Locate and identify every blood parasite.
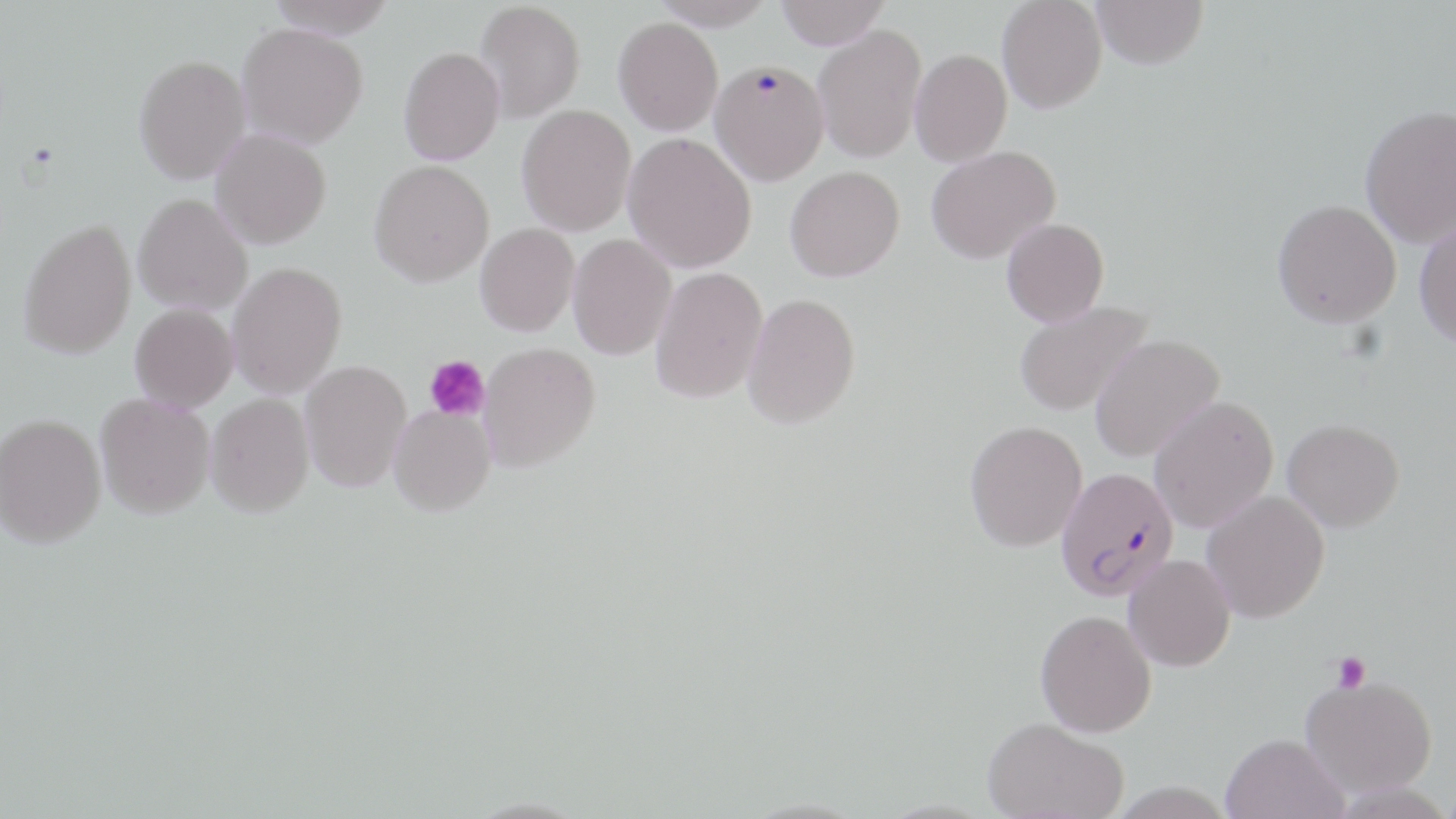

Approximate bounding boxes as named x1/y1/x2/y2 corners in pixels.
Plasmodium falciparum-infected red blood cells: (x1=1056, y1=466, x2=1178, y2=600).
No Plasmodium ovale, Plasmodium malariae, Plasmodium vivax, Babesia divergens, or Trypanosoma brucei observed.

{
  "slide_level_diagnosis": "Plasmodium falciparum",
  "field_of_view": "single",
  "image_size": "1456×819 pixels",
  "platelet_locations": "approximate bounding boxes as named x1/y1/x2/y2 corners in pixels: (x1=424, y1=354, x2=490, y2=422), (x1=1331, y1=651, x2=1369, y2=693)",
  "modality": "optical microscopy",
  "uninfected_red_blood_cell_locations": "approximate bounding boxes as named x1/y1/x2/y2 corners in pixels: (x1=267, y1=0, x2=397, y2=39), (x1=650, y1=0, x2=777, y2=29), (x1=776, y1=0, x2=890, y2=49), (x1=997, y1=0, x2=1107, y2=114), (x1=1091, y1=0, x2=1208, y2=69), (x1=475, y1=1, x2=585, y2=122), (x1=613, y1=17, x2=723, y2=135), (x1=237, y1=22, x2=369, y2=148), (x1=813, y1=24, x2=927, y2=163), (x1=398, y1=47, x2=505, y2=165), (x1=910, y1=48, x2=1012, y2=167), (x1=134, y1=54, x2=251, y2=183), (x1=708, y1=57, x2=827, y2=183), (x1=516, y1=104, x2=636, y2=235), (x1=1360, y1=104, x2=1456, y2=247), (x1=210, y1=128, x2=331, y2=249), (x1=623, y1=132, x2=757, y2=273), (x1=926, y1=145, x2=1060, y2=264), (x1=369, y1=159, x2=494, y2=286), (x1=785, y1=166, x2=905, y2=281), (x1=133, y1=193, x2=252, y2=314), (x1=1272, y1=199, x2=1401, y2=328), (x1=1001, y1=218, x2=1109, y2=327), (x1=19, y1=219, x2=136, y2=360), (x1=1414, y1=219, x2=1456, y2=348), (x1=475, y1=223, x2=579, y2=336), (x1=568, y1=234, x2=676, y2=360), (x1=227, y1=261, x2=347, y2=399), (x1=650, y1=267, x2=768, y2=404), (x1=742, y1=292, x2=861, y2=429), (x1=1014, y1=300, x2=1153, y2=416), (x1=130, y1=303, x2=238, y2=412), (x1=1089, y1=334, x2=1225, y2=462), (x1=478, y1=343, x2=600, y2=472), (x1=300, y1=359, x2=412, y2=493), (x1=95, y1=393, x2=215, y2=519), (x1=206, y1=393, x2=314, y2=517), (x1=1148, y1=395, x2=1279, y2=532), (x1=389, y1=404, x2=496, y2=516), (x1=0, y1=415, x2=106, y2=549), (x1=1282, y1=419, x2=1405, y2=532), (x1=965, y1=420, x2=1087, y2=551), (x1=1201, y1=490, x2=1330, y2=623), (x1=1123, y1=554, x2=1235, y2=672), (x1=1035, y1=609, x2=1156, y2=737), (x1=1300, y1=673, x2=1438, y2=796), (x1=983, y1=717, x2=1128, y2=819), (x1=1220, y1=733, x2=1349, y2=819)",
  "magnification": "1000x",
  "preparation": "thin blood smear",
  "stain": "May-Grünwald-Giemsa"
}